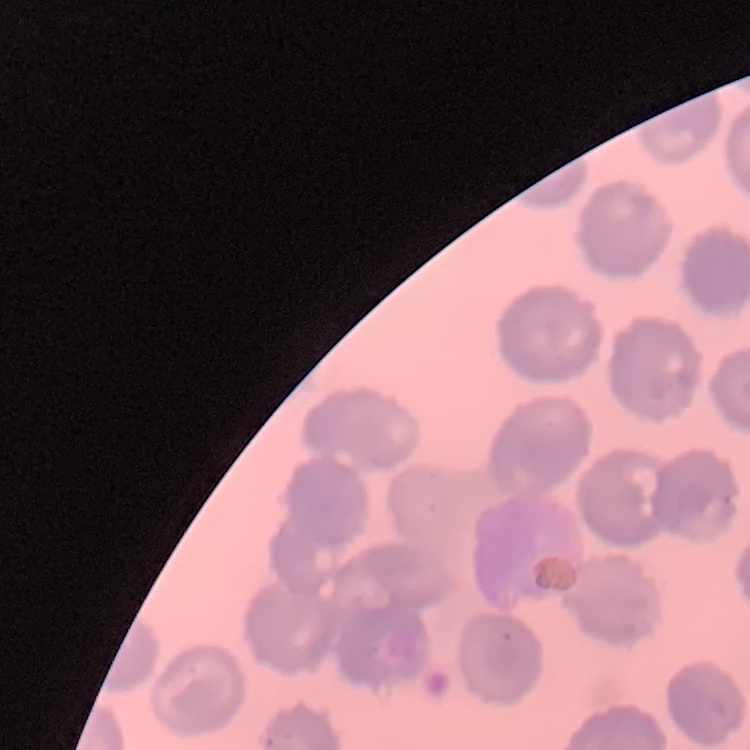 The erythrocytes show no rouleaux formation. One tile cut from a larger photomicrograph. Stained with either Field's or Giemsa. Thin blood smear.